Report the malaria status of this cell.
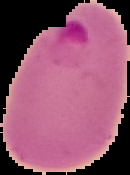
It is parasitized.

The area outside the segmented cell region is set to black. From a thin blood film. Image is 130×175 pixels.